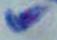

Summary:
  - Identification: Toxoplasma gondii
  - Magnification: 1000x
  - Modality: micrograph